Assess this cell for malaria.
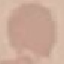

Uninfected.

capture: smartphone through the microscope eyepiece
image_type: automatically extracted cell patch, resized to 64 × 64 pixels
preparation: thin blood film
stain: Giemsa